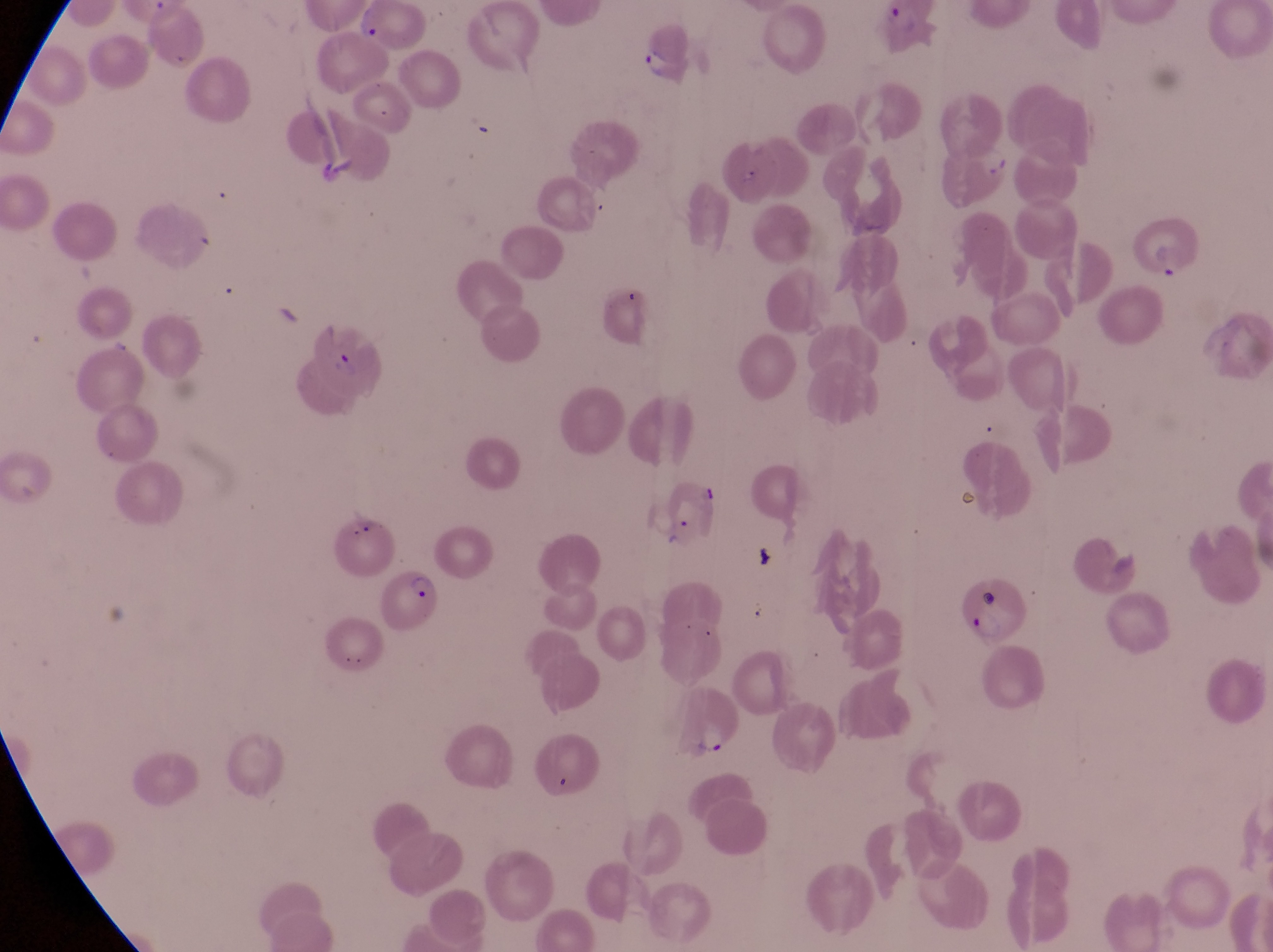

Approximate bounding boxes as [left, top, right, bottom] in pixels. Parasitised red blood cell locations: [632, 23, 695, 88], [1130, 220, 1205, 282], [299, 313, 389, 403], [664, 479, 724, 551], [379, 570, 437, 633], [948, 572, 1031, 647], [669, 679, 744, 762]. Thin blood smear. Collected in Uganda. Magnification of 1000x. Captured by a smartphone held over the eyepiece of an Olympus CX-23 microscope. Image is 1273×952 pixels. Single field of view.